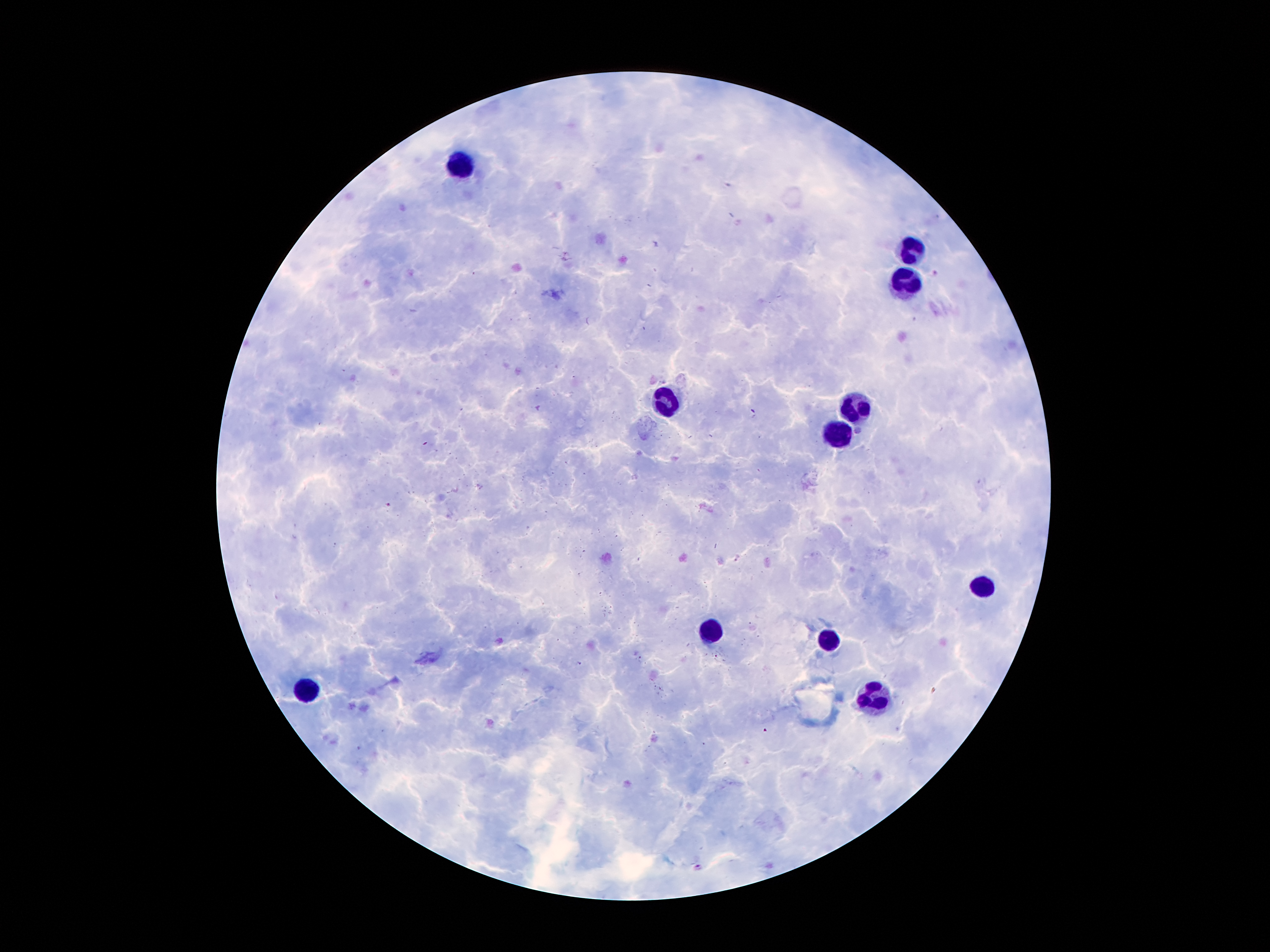

image_size: 1270×952 pixels
magnification: 100x
stain: Giemsa
leukocyte_locations: 'approximate centers as {x, y} in pixels: {460, 167}, {913, 253}, {909, 279}, {663, 405}, {861, 405}, {840, 430}, {986, 589}, {712, 631}, {829, 642}, {309, 690}, {875, 699}'
patient_malaria_status: infected with Plasmodium falciparum
field_of_view: one from this slide
capture: smartphone camera through the microscope eyepiece
plasmodium_parasite_locations: 'approximate centers as {x, y} in pixels: {698, 867}'
preparation: thick peripheral-blood smear